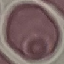

{
  "malaria_status": "uninfected",
  "capture": "smartphone camera at the microscope eyepiece",
  "stain": "Giemsa",
  "preparation": "thin blood smear",
  "image_type": "cell patch, automatically extracted from a larger field of view and resized to 64 × 64 pixels"
}